Classify this cell by malaria status.
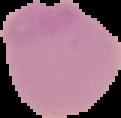
Uninfected.

Image is 121×118 pixels. Segmented cell region on a black background. From a thin blood smear.